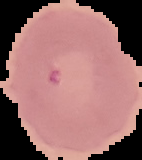
image size = 142×160 pixels
preparation = thin blood film
image type = cell region segmented out of the field of view; surrounding area masked to black
malaria status = parasitized